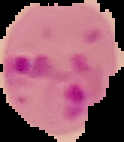
{
  "malaria_status": "parasitized",
  "image_type": "segmented cell region with the area outside set to black",
  "image_size": "124×142 pixels",
  "preparation": "thin blood film"
}